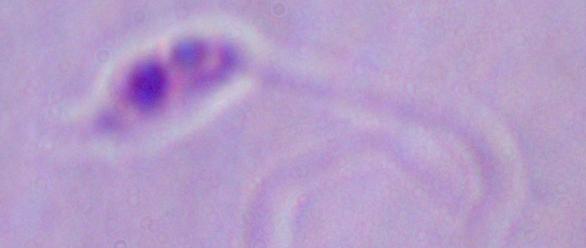

Summary:
  - Modality: photomicrograph
  - Identification: Leishmania
  - Magnification: 1000x